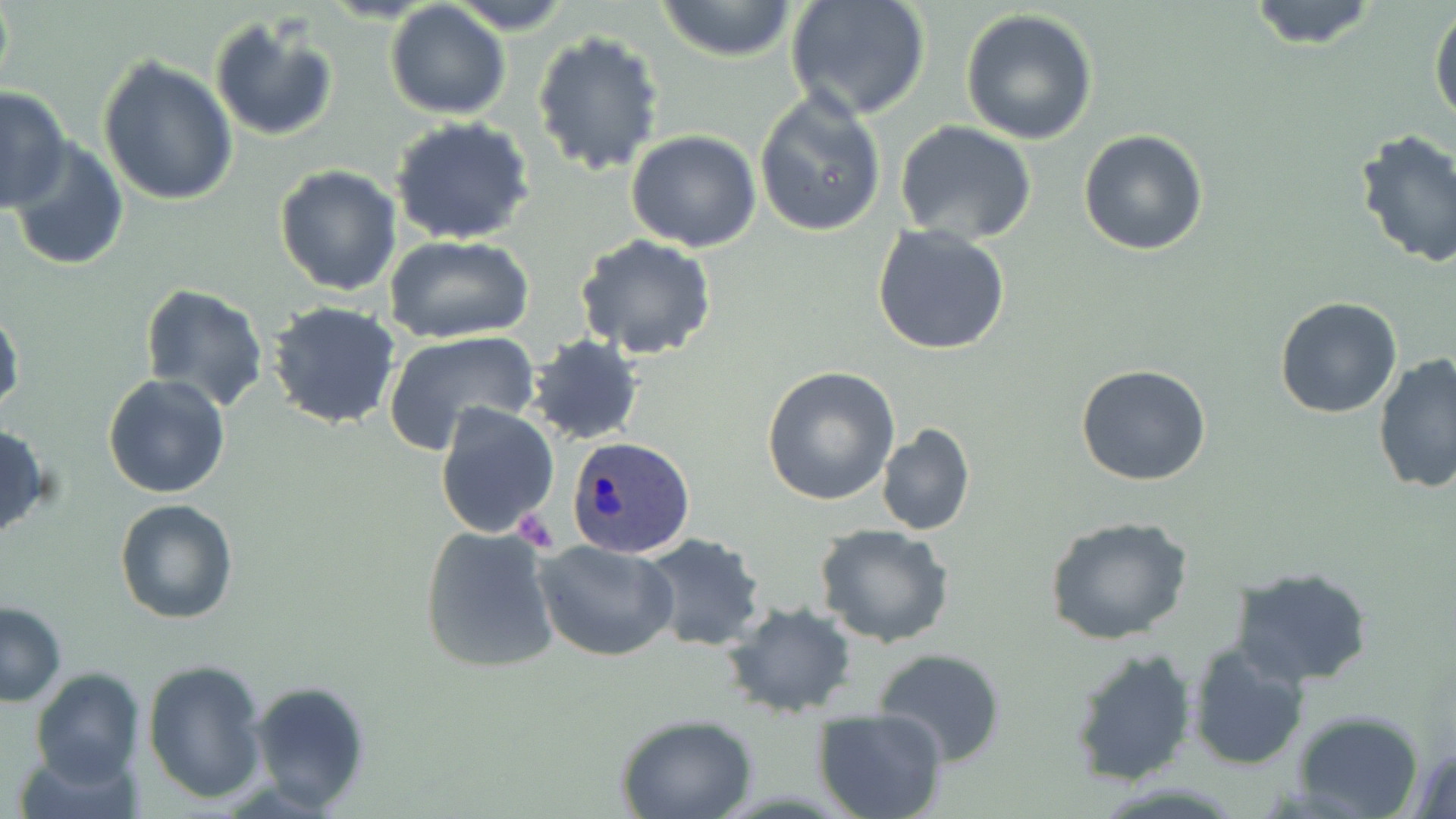
{
  "slide_level_diagnosis": "Plasmodium ovale",
  "platelet_locations": "approximate bounding boxes as [x1, y1, x2, y2] in pixels: [515, 507, 554, 553]",
  "plasmodium_ovale_infected_red_blood_cell_locations": "approximate bounding boxes as [x1, y1, x2, y2] in pixels: [568, 434, 696, 559]",
  "modality": "optical microscopy",
  "uninfected_red_blood_cell_locations": "approximate bounding boxes as [x1, y1, x2, y2] in pixels: [444, 0, 578, 35], [654, 0, 802, 63], [786, 0, 932, 121], [1245, 0, 1382, 51], [384, 2, 510, 119], [958, 7, 1100, 145], [1429, 7, 1456, 130], [209, 17, 336, 143], [532, 29, 665, 177], [98, 54, 237, 207], [0, 85, 71, 209], [754, 90, 887, 239], [388, 117, 537, 245], [894, 121, 1038, 247], [626, 129, 762, 252], [1078, 129, 1209, 255], [1353, 129, 1456, 270], [8, 138, 130, 272], [274, 164, 403, 297], [871, 224, 1011, 357], [574, 233, 717, 360], [385, 236, 533, 345], [138, 283, 270, 414], [1275, 298, 1404, 419], [267, 300, 402, 430], [0, 307, 23, 417], [385, 329, 538, 454], [526, 335, 645, 446], [1373, 351, 1455, 494], [1076, 363, 1211, 486], [760, 365, 900, 507], [103, 372, 232, 498], [434, 403, 562, 539], [0, 422, 51, 543], [876, 425, 975, 536], [114, 499, 238, 624], [1044, 516, 1194, 647], [419, 524, 561, 675], [815, 525, 955, 648], [635, 533, 767, 654], [533, 538, 678, 660], [1230, 567, 1375, 688], [1, 599, 65, 706], [723, 602, 858, 718], [1186, 643, 1309, 769], [874, 646, 1006, 768], [1068, 646, 1197, 789], [143, 659, 269, 804], [30, 669, 144, 785], [249, 680, 373, 812], [814, 708, 948, 819], [1296, 713, 1424, 818], [614, 714, 757, 819], [1407, 742, 1456, 819], [13, 743, 146, 819]",
  "image_size": "1456×819 pixels",
  "field_of_view": "single",
  "magnification": "1000x",
  "preparation": "thin blood smear",
  "stain": "May-Grünwald-Giemsa"
}